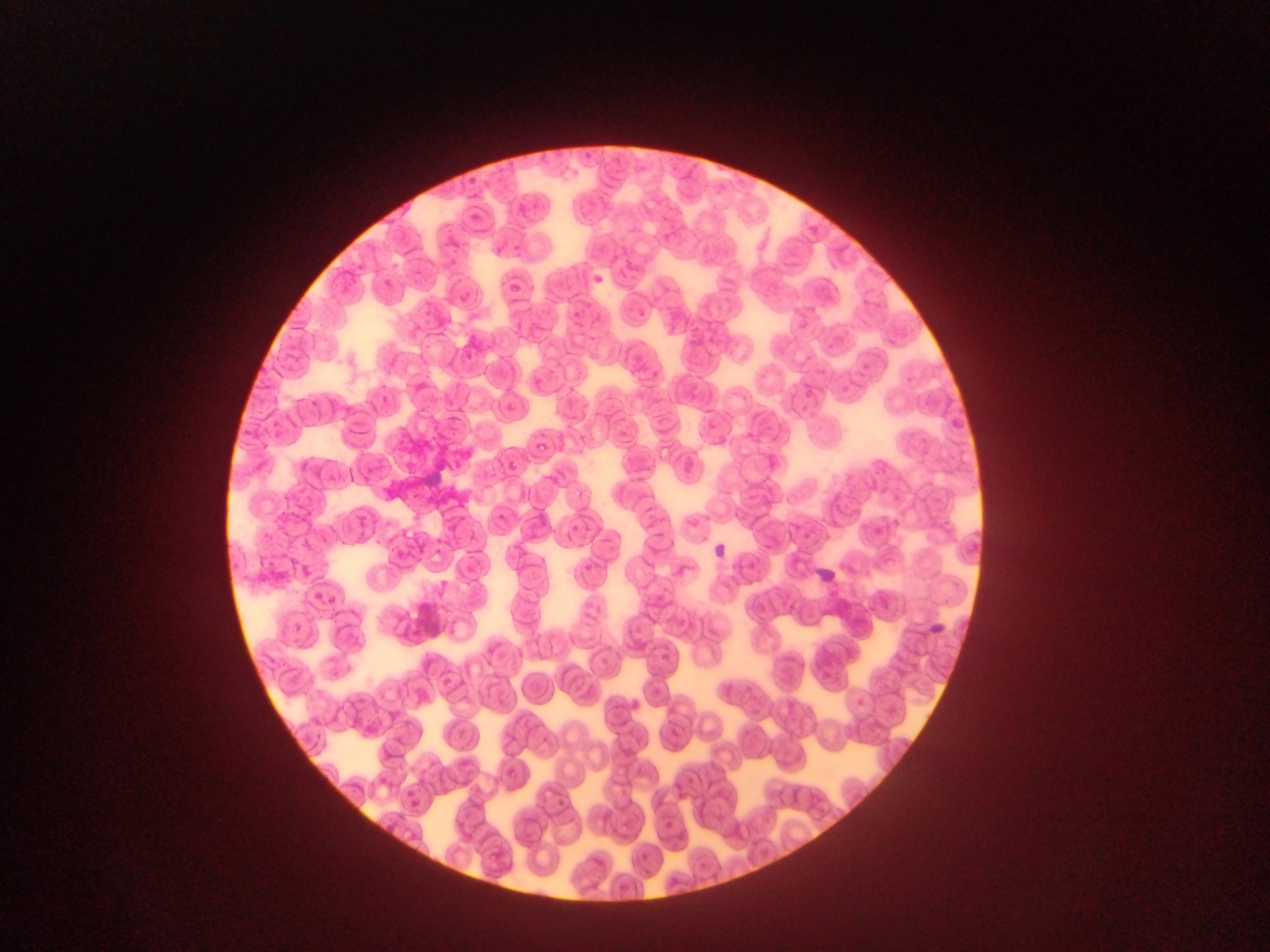 Approximate bounding boxes as left top right bottom in pixels. Malaria parasite locations: 502 280 524 300; 532 441 550 457; 502 457 522 476; 570 524 579 533; 402 793 423 813. Sample from Ghana. Mobile-phone photograph taken through the microscope. Image is 1270×952 pixels. One field of view. Thin blood smear.